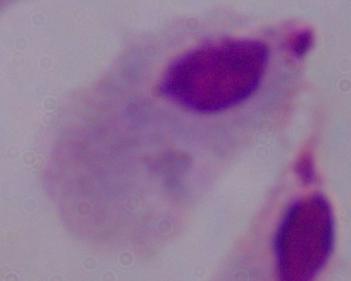

Captured at 1000x magnification. Photomicrograph. A trichomonad is seen.